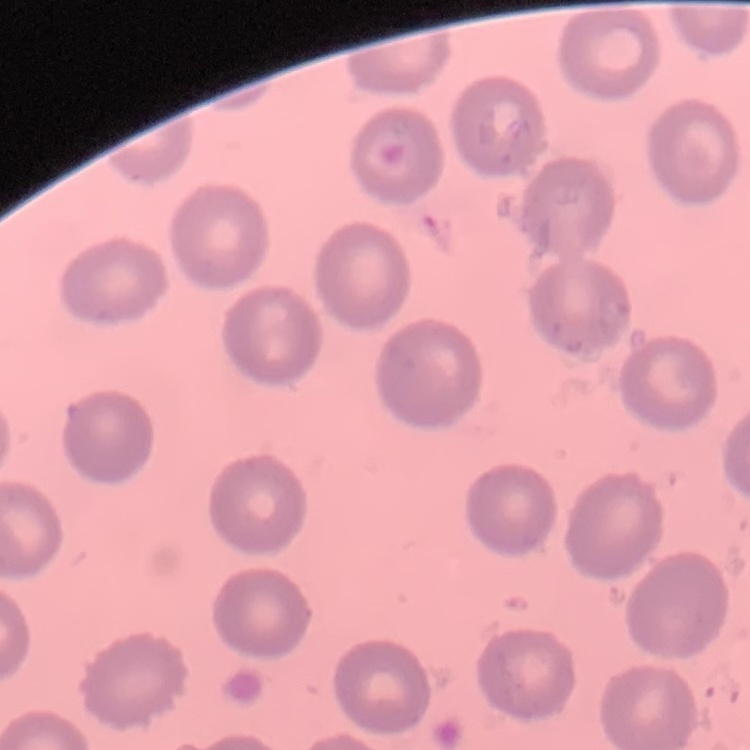

erythrocyte_morphology: no rouleaux formation
stain: Field's or Giemsa
preparation: thin blood smear
image_type: square crop of a larger photomicrograph